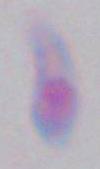 1000x magnification. Micrograph. Toxoplasma gondii is shown.